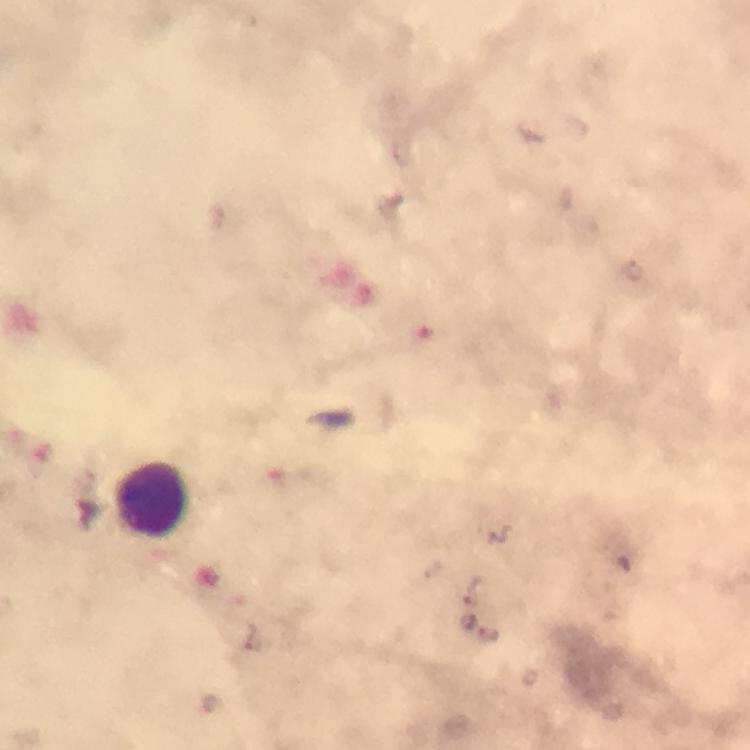

Approximate object centers, in pixels from the top-left corner.
Summary:
  - Leukocyte locations: (x=152, y=500)
  - Preparation: thick blood smear
  - Capture: smartphone photograph through a microscope
  - Context: from a diagnostic examination for malaria
  - Plasmodium parasites: none detected
  - Stain: Giemsa
  - Cropped from: one field of view
  - Magnification: 100x
  - Image size: 750×750 pixels
  - Immersion oil: used